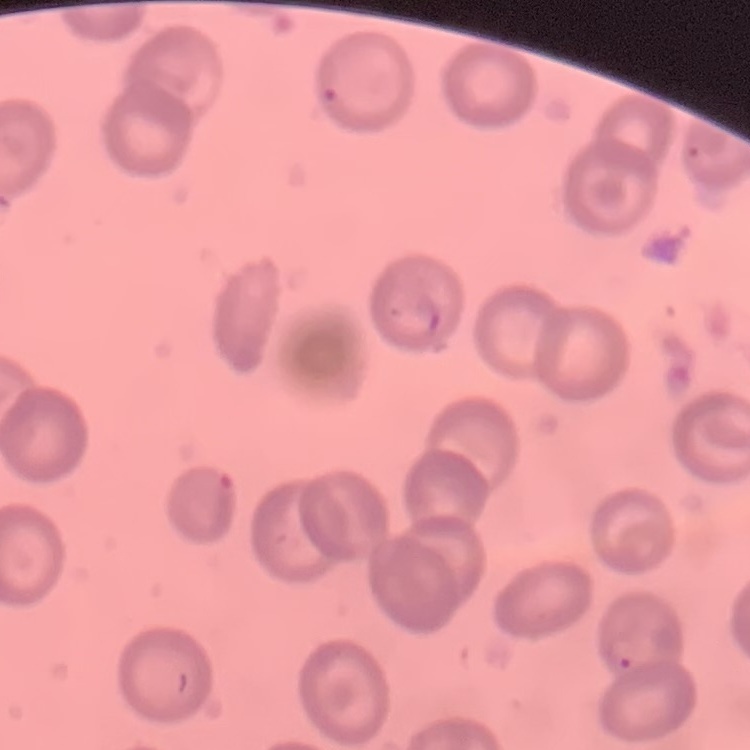

Summary:
  - Erythrocyte morphology: no rouleaux formation
  - Image type: square crop of a larger photomicrograph
  - Stain: Field's or Giemsa
  - Preparation: thin blood film